Give a bounding box for every Plasmodium parasite.
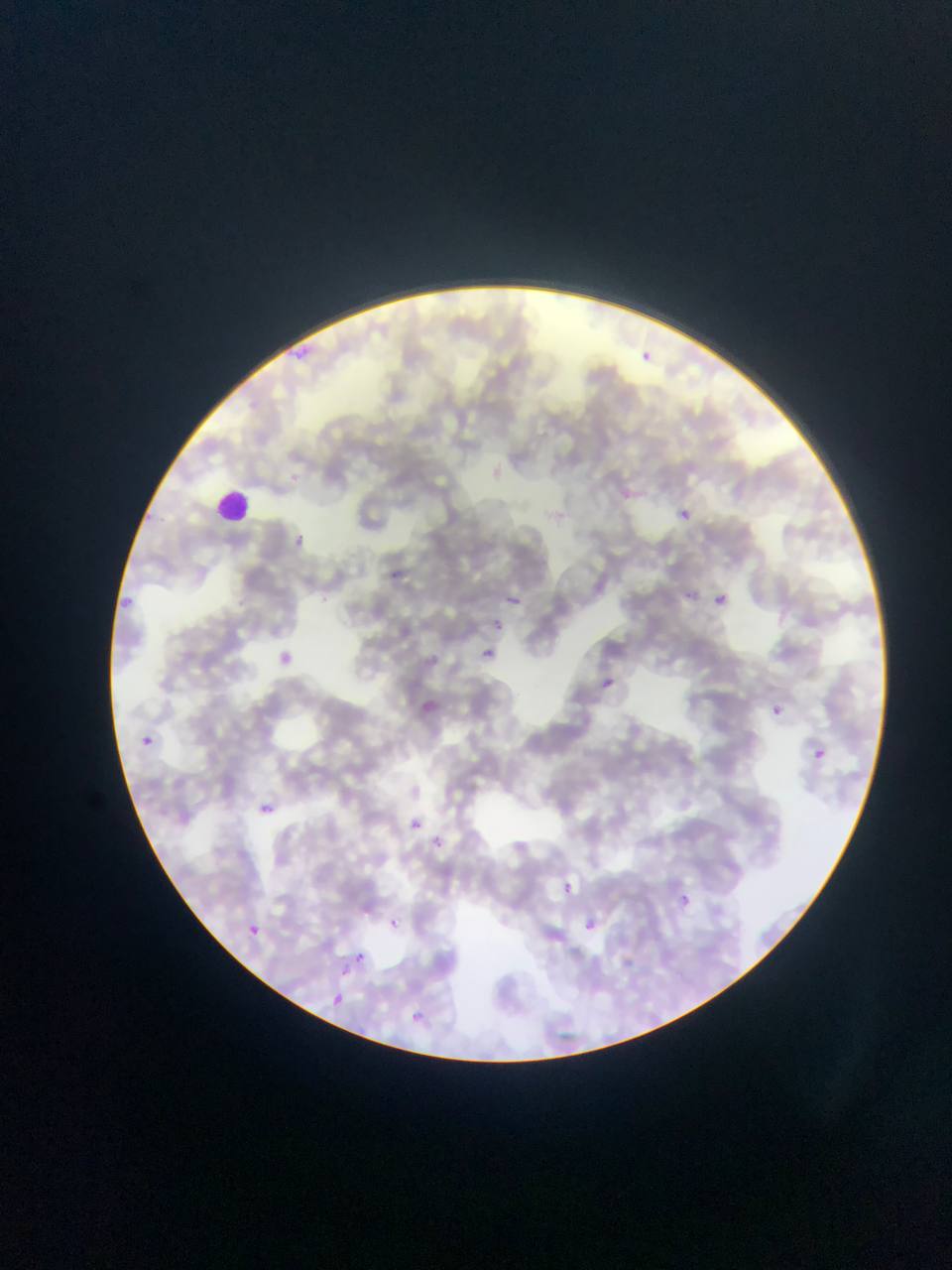
Approximate bounding boxes as {left, top, right, bottom} in pixels.
Plasmodium parasites: {302, 347, 310, 355}, {294, 351, 307, 358}, {641, 352, 654, 360}, {621, 489, 634, 500}, {681, 508, 692, 519}, {683, 591, 701, 600}, {715, 594, 728, 604}, {507, 597, 520, 606}, {497, 618, 508, 632}, {484, 647, 496, 660}, {604, 679, 619, 688}, {773, 702, 785, 714}, {141, 736, 154, 747}, {812, 749, 827, 759}, {261, 804, 275, 813}, {413, 822, 421, 830}, {431, 835, 442, 849}, {568, 883, 574, 893}, {680, 892, 693, 910}, {587, 918, 597, 931}, {391, 920, 407, 933}, {252, 926, 262, 936}, {355, 955, 369, 967}, {345, 967, 351, 978}, {328, 992, 344, 1008}.

Summary:
  - Leukocyte locations: {215, 489, 255, 524}
  - Image size: 952×1270 pixels
  - Field of view: single
  - Preparation: thin blood film
  - Country: Ghana
  - Capture: mobile-phone photograph through a microscope